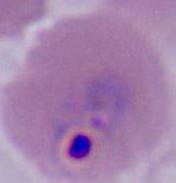
A Plasmodium parasite is shown. Captured at either 400x or 1000x magnification. Micrograph.